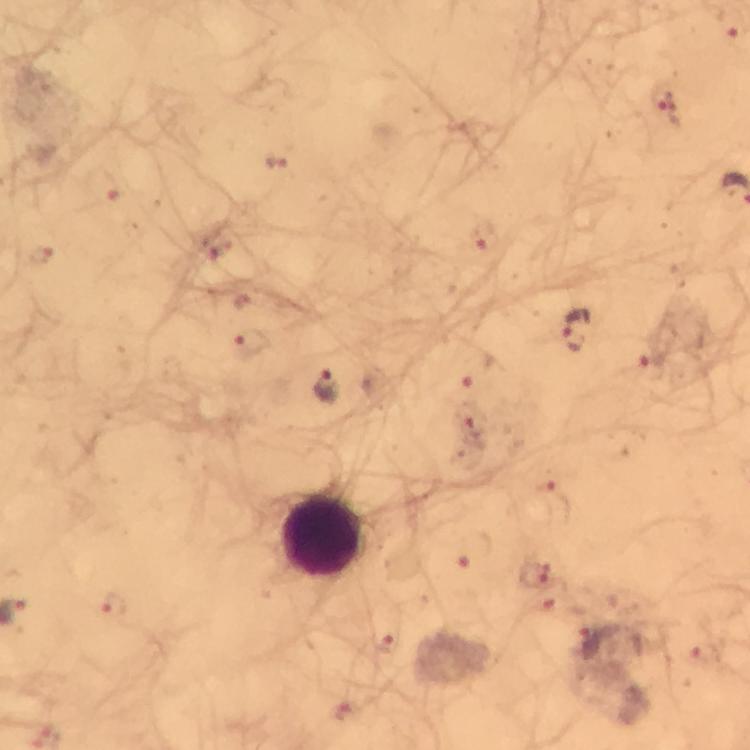

Approximate object centers, in pixels from the top-left corner.
Summary:
  - Plasmodium parasite locations: (x=665, y=105), (x=277, y=161), (x=105, y=187), (x=484, y=238), (x=220, y=249), (x=38, y=258), (x=579, y=331), (x=253, y=344), (x=650, y=356), (x=479, y=371), (x=328, y=388), (x=472, y=426), (x=557, y=496), (x=474, y=551), (x=535, y=577), (x=115, y=606), (x=557, y=607), (x=390, y=644), (x=592, y=646), (x=703, y=655), (x=345, y=714)
  - Leukocyte locations: (x=322, y=537)
  - Stain: Giemsa
  - Magnification: 100x
  - Image size: 750×750 pixels
  - Immersion oil: applied
  - Preparation: thick blood smear
  - Capture: smartphone photograph through a microscope
  - Context: from a diagnostic examination for malaria
  - Cropped from: a single field of view